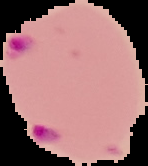

From a thin blood film. Image is 148×166 pixels. Cell region segmented out of the field of view; the surrounding area is masked to black. Malaria status: parasitized.